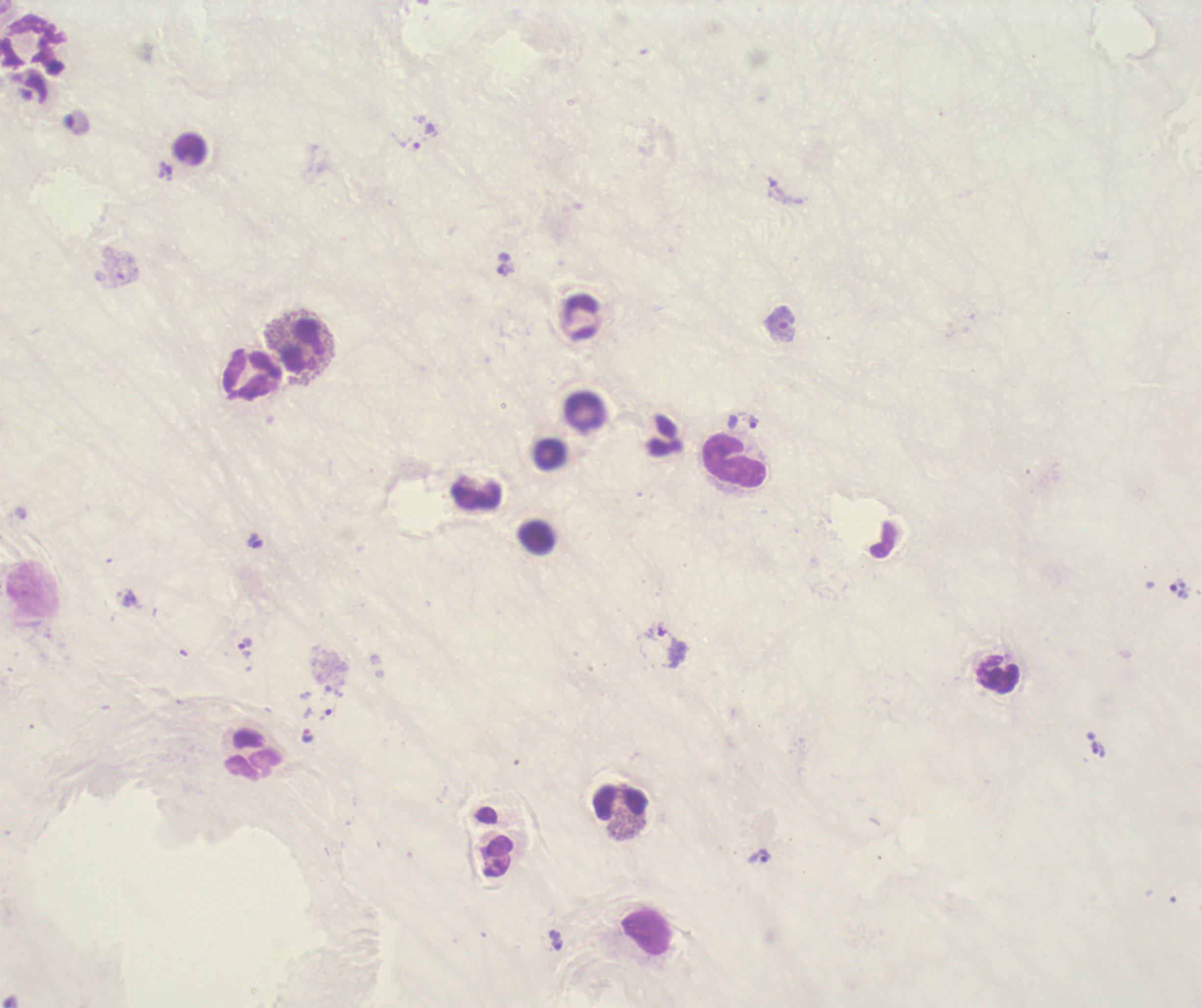 Approximate centers as [x, y] in pixels. Leukocyte locations: [31, 41], [302, 346], [252, 375], [733, 462], [999, 674], [254, 754], [621, 803]. Trophozoite locations: [424, 137], [506, 270], [780, 323], [753, 422], [255, 541], [1177, 588], [1098, 749], [759, 856]. Romanowsky-stained preparation. Image is 1202×1008 pixels. Previously used in an actual diagnosis. Coloration quality: bad. Thick blood film. Background quality: poor. One field from this slide. Result: Plasmodium parasites detected. Captured at 100x magnification.